Comment on the morphology of the erythrocytes.
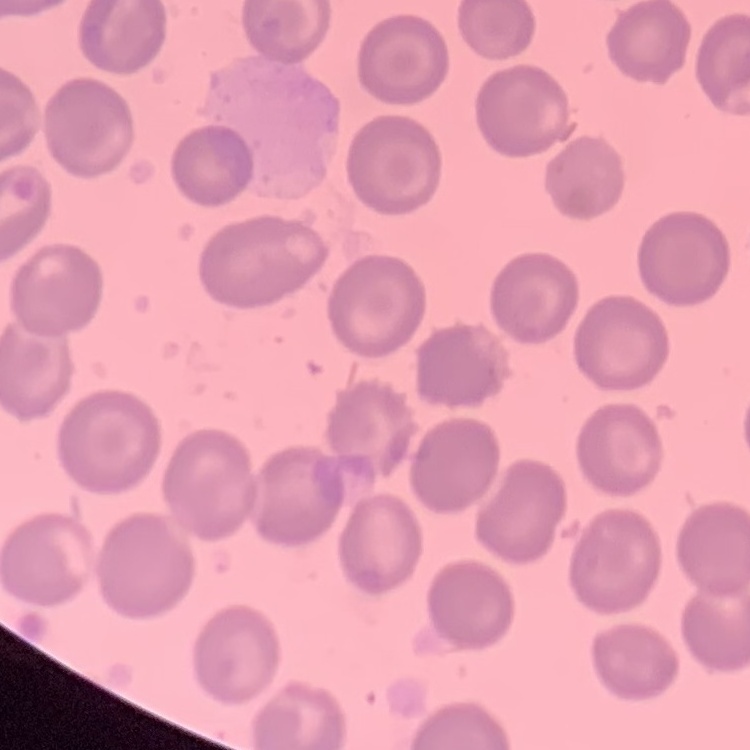
No rouleaux formation.

Summary:
  - Image type: square crop of a larger photomicrograph
  - Preparation: thin peripheral smear
  - Stain: Field's or Giemsa